Locate every leukocyte (white blood cell).
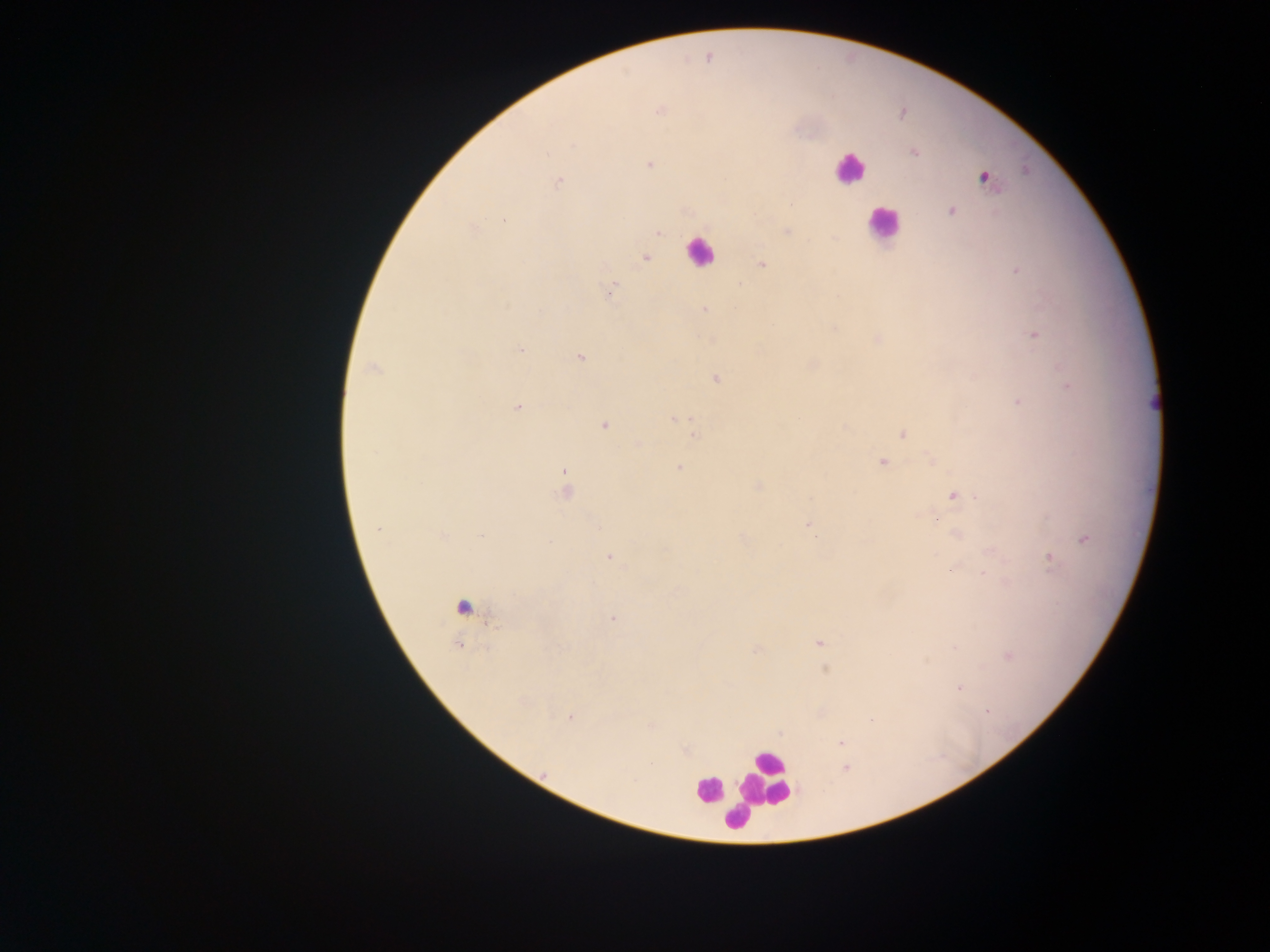

Approximate centers as {x, y} in pixels.
Leukocytes: {849, 169}, {882, 223}, {699, 251}, {767, 778}, {708, 788}, {736, 819}.

Malaria parasite locations: {708, 57}, {660, 111}, {903, 113}, {913, 152}, {650, 164}, {985, 177}, {559, 183}, {951, 211}, {505, 220}, {786, 231}, {658, 232}, {646, 258}, {761, 263}, {1016, 270}, {612, 290}, {704, 309}, {1034, 335}, {521, 349}, {580, 357}, {373, 367}, {716, 379}, {1069, 385}, {1018, 402}, {517, 407}, {678, 419}, {605, 425}, {902, 433}, {696, 436}, {638, 445}, {931, 460}, {882, 462}, {679, 468}, {565, 472}, {757, 486}, {566, 491}, {953, 496}, {809, 526}, {378, 529}, {956, 534}, {441, 535}, {815, 535}, {483, 536}, {1085, 540}, {550, 541}, {610, 557}, {1050, 559}, {951, 570}, {983, 574}, {463, 607}, {613, 619}, {820, 642}, {457, 646}, {955, 648}, {757, 651}, {1009, 656}, {826, 670}, {959, 688}, {987, 712}, {570, 717}, {872, 721}, {652, 725}, {841, 743}, {652, 763}, {845, 768}, {634, 779}. Image is 1270×952 pixels. Single field of view. Thick blood smear. Mobile-phone photograph taken through the microscope. Collected in Ghana.